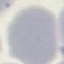

malaria status = uninfected
stain = Giemsa
image type = cell patch, automatically extracted from a larger field of view and resized to 64 × 64 pixels
preparation = thin blood smear
capture = smartphone through the microscope eyepiece